State the preparation type.
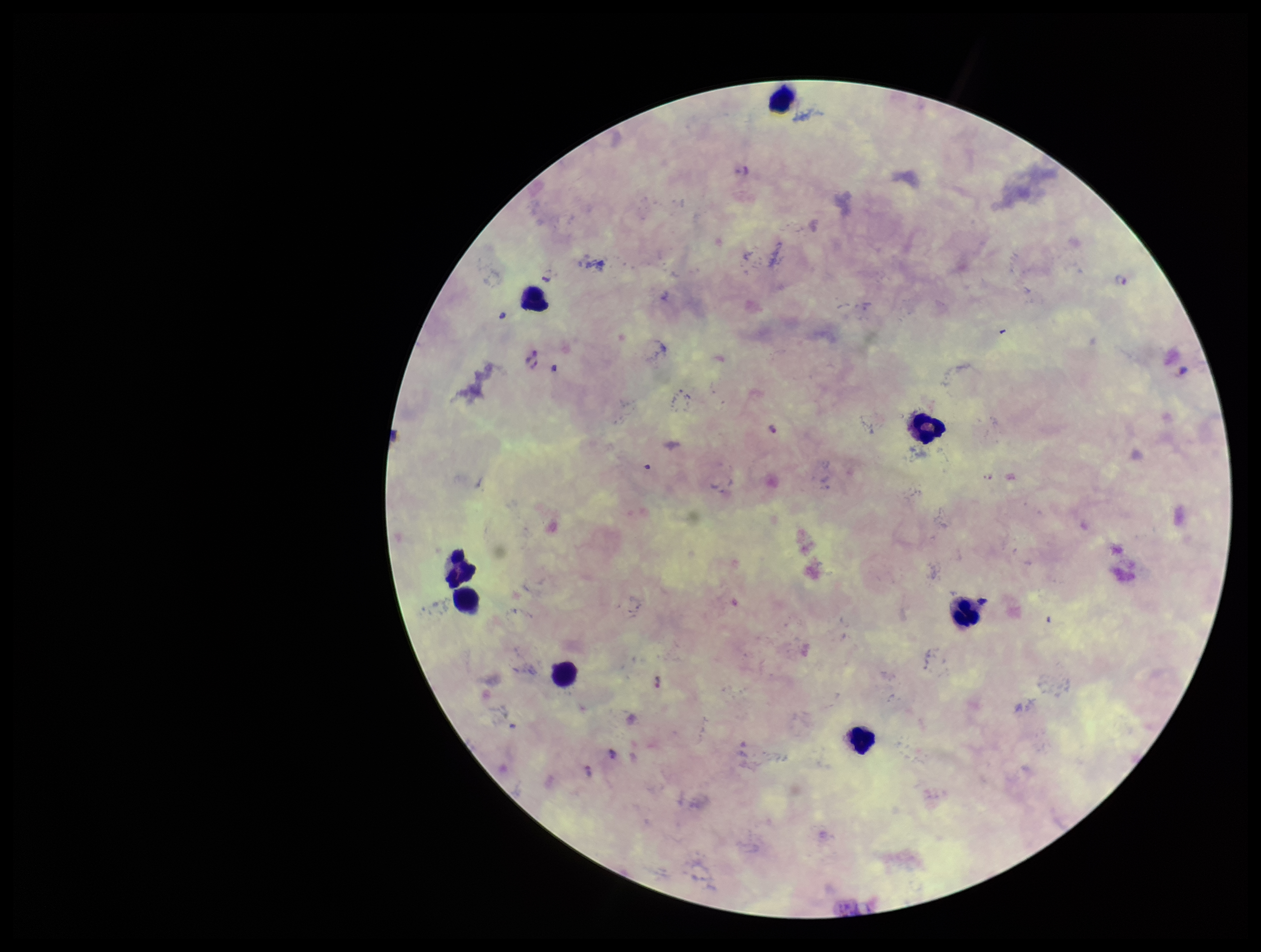
It is a thick blood smear.

Single field of view. Parasite count: 2. Species reported for this patient: Plasmodium falciparum. Plasmodium parasites: detected. Image is 1261×952 pixels. Patient malaria status: infected. Smartphone photograph taken through the eyepiece of a microscope. Giemsa stain. Leukocyte count: 8.